Identify the parasite.
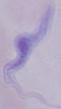
This is a trypanosome.

Photomicrograph. 1000x magnification.